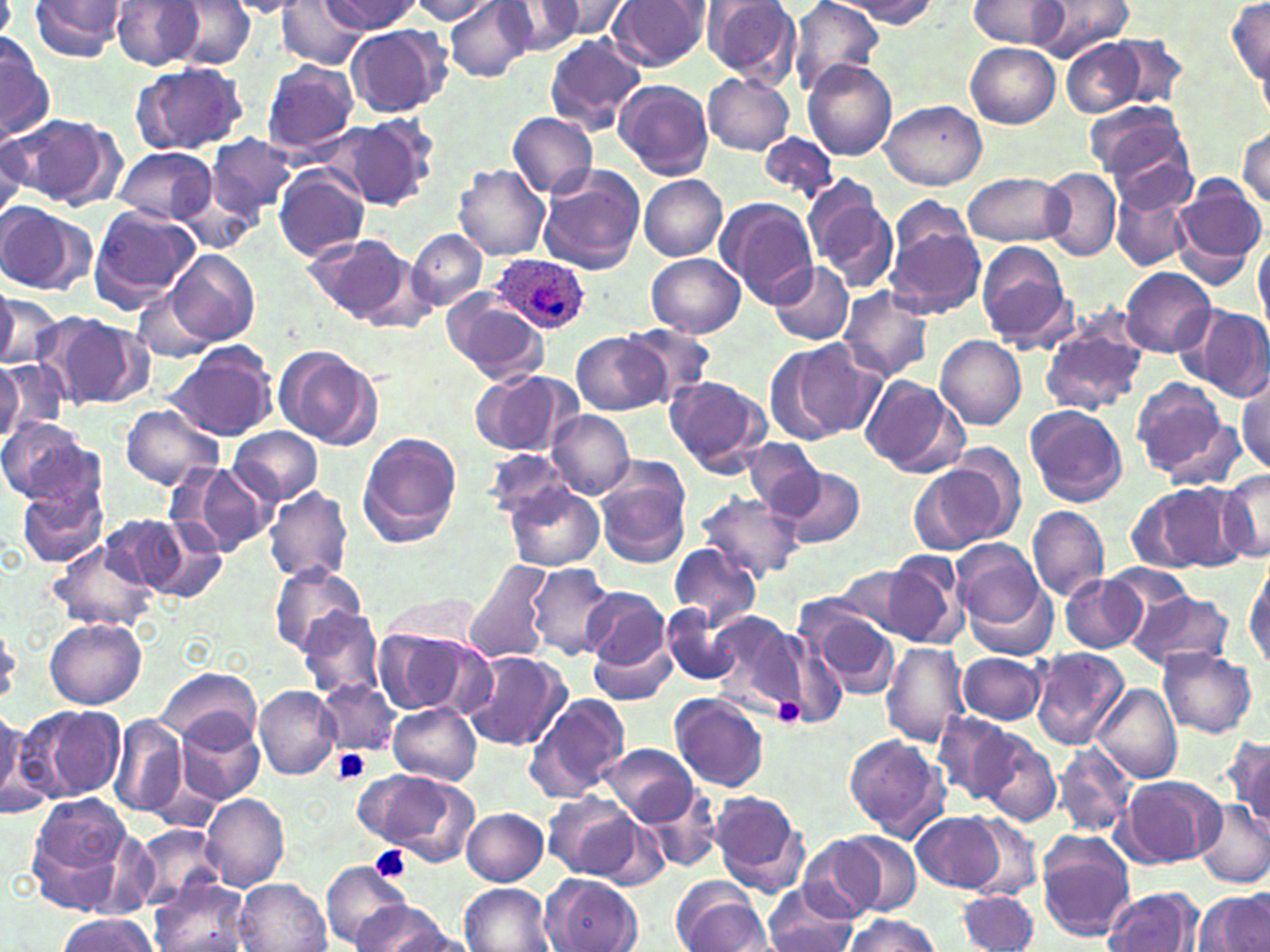
Summary:
  - Coordinate format: approximate bounding boxes as (x1, y1, x2, y2) in pixels
  - Plasmodium ovale-infected red blood cell locations: (488, 253, 589, 337)
  - Platelet locations: (772, 695, 806, 726), (333, 748, 373, 785), (371, 846, 412, 882)
  - Uninfected red blood cell locations: (28, 0, 128, 61), (170, 0, 256, 68), (323, 0, 422, 34), (408, 0, 497, 23), (445, 0, 536, 82), (542, 0, 632, 40), (610, 0, 709, 72), (786, 0, 886, 93), (835, 0, 940, 28), (967, 0, 1072, 50), (1032, 0, 1135, 58), (1227, 0, 1269, 92), (225, 1, 311, 17), (275, 1, 368, 68), (501, 1, 585, 57), (701, 1, 801, 84), (109, 2, 210, 70), (345, 24, 452, 119), (1, 33, 56, 140), (1103, 33, 1190, 109), (543, 34, 645, 133), (1061, 37, 1145, 116), (965, 43, 1060, 129), (128, 60, 251, 156), (261, 60, 359, 154), (802, 60, 897, 161), (703, 74, 794, 154), (614, 79, 715, 180), (882, 100, 986, 190), (1089, 104, 1198, 205), (506, 112, 599, 198), (5, 114, 119, 206), (324, 119, 436, 210), (0, 126, 31, 218), (1235, 126, 1270, 209), (206, 133, 297, 222), (275, 133, 428, 250), (757, 134, 837, 207), (112, 146, 216, 226), (453, 164, 550, 260), (273, 166, 370, 262), (1041, 167, 1121, 261), (537, 168, 645, 275), (963, 171, 1069, 247), (639, 176, 728, 261), (1171, 177, 1266, 283), (808, 186, 900, 295), (1112, 186, 1196, 272), (172, 188, 263, 255), (892, 194, 973, 259), (717, 196, 820, 306), (0, 203, 94, 296), (87, 206, 201, 312), (884, 223, 986, 318), (408, 229, 487, 312), (304, 233, 420, 327), (1252, 233, 1269, 328), (977, 241, 1074, 349), (166, 249, 260, 345), (646, 253, 745, 339), (769, 262, 854, 345), (1119, 267, 1216, 357), (838, 285, 936, 383), (132, 288, 218, 363), (0, 292, 62, 367), (444, 293, 549, 383), (1179, 304, 1269, 401), (44, 313, 152, 410), (1039, 322, 1147, 415), (621, 323, 716, 404), (573, 332, 667, 416), (935, 335, 1027, 430), (771, 338, 868, 443), (161, 345, 276, 442), (274, 346, 383, 450), (0, 357, 66, 442), (0, 359, 25, 444), (470, 371, 580, 456), (664, 374, 771, 478), (1235, 374, 1269, 476), (860, 375, 967, 478), (1130, 377, 1239, 485), (119, 403, 224, 490), (1025, 406, 1127, 507), (547, 410, 635, 499), (0, 418, 100, 505), (229, 426, 323, 507), (358, 432, 463, 548), (744, 439, 826, 519), (484, 448, 577, 522), (919, 453, 1021, 551), (592, 462, 692, 568), (187, 463, 280, 556), (777, 465, 868, 550), (1214, 470, 1270, 563), (16, 476, 109, 570), (504, 483, 605, 572), (1129, 483, 1241, 574), (264, 486, 353, 584), (694, 492, 804, 581), (1028, 506, 1109, 602), (100, 513, 192, 595), (979, 518, 1076, 636), (147, 520, 226, 604), (52, 543, 158, 630), (668, 543, 762, 629), (881, 550, 967, 648), (956, 550, 1058, 659), (463, 558, 555, 665), (1246, 558, 1270, 672), (526, 563, 617, 659), (269, 564, 370, 654), (1103, 564, 1197, 633), (828, 566, 925, 638), (1060, 574, 1148, 654), (581, 586, 673, 677), (1125, 587, 1234, 673), (383, 591, 477, 649), (799, 600, 902, 701), (661, 603, 743, 686), (296, 607, 384, 701), (708, 611, 804, 713), (44, 618, 147, 709), (0, 622, 21, 710), (373, 628, 491, 717), (590, 633, 676, 706), (880, 641, 971, 748), (1030, 647, 1129, 750), (1157, 647, 1258, 737), (461, 651, 573, 750), (959, 652, 1047, 726), (157, 667, 260, 749), (316, 679, 401, 756), (1093, 683, 1182, 784), (254, 686, 341, 780), (669, 692, 769, 792), (525, 694, 631, 801), (18, 703, 126, 806), (389, 704, 481, 784), (0, 705, 40, 819), (175, 713, 265, 804), (932, 713, 1018, 806), (109, 715, 187, 820), (973, 731, 1061, 827), (842, 733, 953, 842), (1228, 735, 1270, 832), (600, 743, 698, 825), (1052, 744, 1137, 839), (356, 768, 479, 864), (1120, 776, 1225, 866), (641, 786, 723, 874), (710, 790, 812, 897), (200, 793, 289, 893), (542, 793, 646, 882), (26, 796, 137, 913), (1195, 801, 1270, 889), (461, 807, 549, 885), (911, 811, 1012, 893), (964, 817, 1043, 900), (133, 823, 226, 907), (1036, 831, 1138, 941), (799, 833, 914, 916), (320, 861, 412, 948), (543, 873, 644, 951), (671, 876, 768, 952), (234, 879, 331, 952), (149, 881, 254, 952), (459, 883, 554, 952), (761, 887, 864, 952), (1102, 887, 1203, 952), (1197, 890, 1270, 951), (956, 892, 1041, 952), (350, 901, 454, 952), (53, 914, 158, 951), (840, 914, 941, 952), (764, 918, 858, 950), (386, 927, 481, 952)
  - Slide-level diagnosis: Plasmodium ovale
  - Preparation: thin blood film
  - Field of view: one of a larger specimen
  - Magnification: 1000x
  - Image size: 1270×952 pixels
  - Stain: May-Grünwald-Giemsa
  - Modality: light microscopy